Describe the morphology of the erythrocytes.
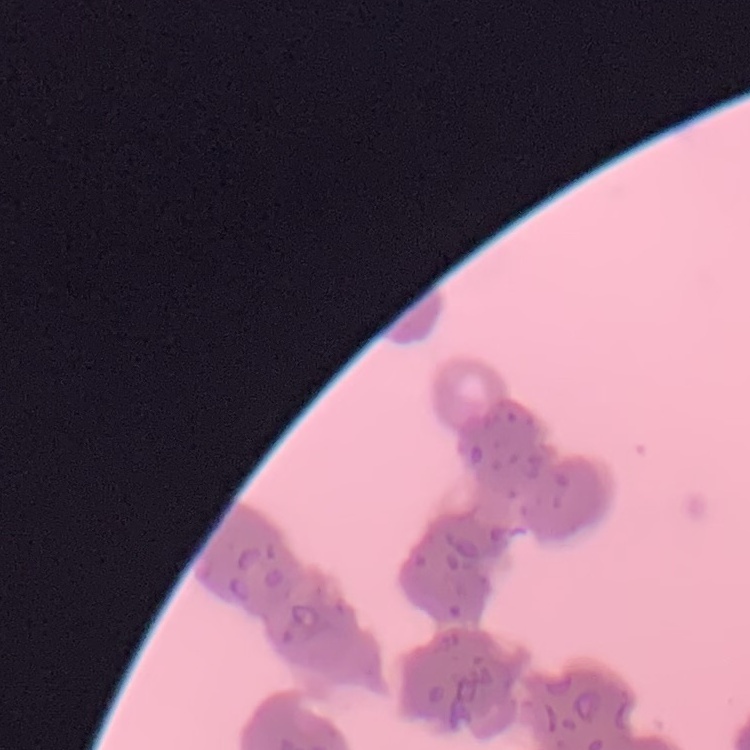
They show rouleaux formation.

{
  "image_type": "one tile cut from a larger photomicrograph",
  "stain": "Field's or Giemsa",
  "preparation": "thin blood film"
}